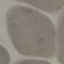

malaria status = uninfected
stain = Giemsa
preparation = thin smear
capture = smartphone through the microscope eyepiece
image type = automatically extracted cell patch, resized to 64 × 64 pixels